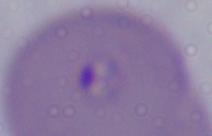
1000x magnification. A Babesia parasite is seen. Photomicrograph.